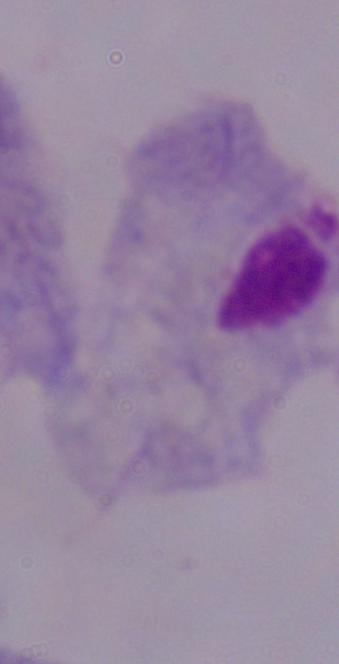
magnification = 1000x
modality = micrograph
identification = trichomonad